Report the malaria status of this cell.
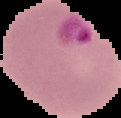
Parasitized.

preparation = thin blood film
image type = cell region segmented out of the field of view; surrounding area masked to black
image size = 121×118 pixels